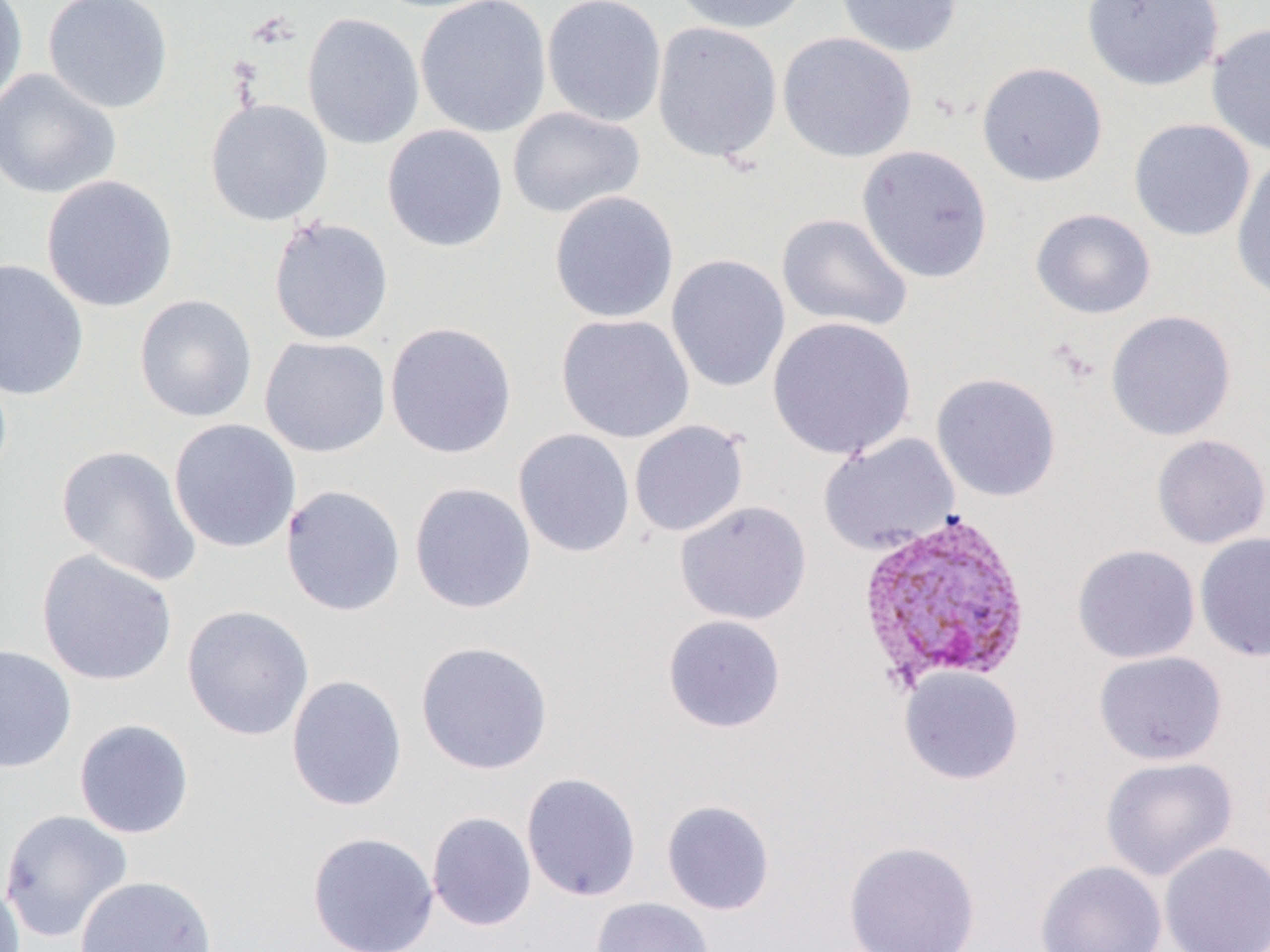

Summary:
  - Coordinate format: approximate bounding boxes as named x1/y1/x2/y2 corners in pixels
  - Uninfected red blood cell locations: (x1=0, y1=0, x2=29, y2=113), (x1=42, y1=0, x2=174, y2=115), (x1=414, y1=0, x2=552, y2=138), (x1=541, y1=0, x2=667, y2=128), (x1=670, y1=0, x2=812, y2=35), (x1=835, y1=0, x2=963, y2=58), (x1=1080, y1=0, x2=1224, y2=91), (x1=302, y1=12, x2=425, y2=150), (x1=651, y1=21, x2=783, y2=165), (x1=1206, y1=22, x2=1270, y2=157), (x1=777, y1=32, x2=917, y2=163), (x1=976, y1=61, x2=1108, y2=187), (x1=0, y1=69, x2=121, y2=200), (x1=205, y1=98, x2=334, y2=227), (x1=506, y1=106, x2=645, y2=219), (x1=1128, y1=118, x2=1256, y2=242), (x1=381, y1=124, x2=508, y2=252), (x1=856, y1=145, x2=994, y2=283), (x1=1231, y1=155, x2=1270, y2=303), (x1=40, y1=175, x2=178, y2=313), (x1=548, y1=191, x2=679, y2=324), (x1=1029, y1=208, x2=1157, y2=320), (x1=775, y1=212, x2=914, y2=333), (x1=268, y1=216, x2=394, y2=345), (x1=666, y1=253, x2=791, y2=392), (x1=0, y1=258, x2=89, y2=401), (x1=134, y1=294, x2=258, y2=423), (x1=1105, y1=310, x2=1237, y2=442), (x1=556, y1=313, x2=695, y2=443), (x1=767, y1=316, x2=916, y2=460), (x1=384, y1=321, x2=517, y2=460), (x1=259, y1=336, x2=391, y2=458), (x1=931, y1=372, x2=1061, y2=502), (x1=168, y1=418, x2=301, y2=554), (x1=629, y1=420, x2=749, y2=538), (x1=513, y1=428, x2=635, y2=558), (x1=818, y1=432, x2=961, y2=555), (x1=1151, y1=434, x2=1270, y2=549), (x1=55, y1=444, x2=202, y2=587), (x1=409, y1=482, x2=537, y2=614), (x1=280, y1=484, x2=407, y2=617), (x1=674, y1=500, x2=812, y2=625), (x1=1194, y1=531, x2=1270, y2=662), (x1=1072, y1=544, x2=1201, y2=664), (x1=35, y1=549, x2=179, y2=686), (x1=181, y1=604, x2=315, y2=741), (x1=662, y1=614, x2=786, y2=733), (x1=415, y1=640, x2=554, y2=776), (x1=0, y1=643, x2=78, y2=774), (x1=1093, y1=650, x2=1228, y2=765), (x1=899, y1=666, x2=1024, y2=785), (x1=285, y1=673, x2=408, y2=811), (x1=73, y1=718, x2=195, y2=839), (x1=1100, y1=755, x2=1238, y2=881), (x1=521, y1=772, x2=642, y2=902), (x1=661, y1=799, x2=775, y2=916), (x1=0, y1=809, x2=134, y2=943), (x1=426, y1=811, x2=537, y2=931), (x1=307, y1=831, x2=439, y2=952), (x1=843, y1=840, x2=981, y2=952), (x1=1158, y1=841, x2=1270, y2=952), (x1=1035, y1=859, x2=1167, y2=952), (x1=74, y1=874, x2=218, y2=952), (x1=0, y1=875, x2=26, y2=952), (x1=590, y1=896, x2=715, y2=952)
  - Plasmodium vivax-infected red blood cell locations: (x1=855, y1=509, x2=1033, y2=690)
  - Slide-level diagnosis: Plasmodium vivax
  - Field of view: single
  - Image size: 1270×952 pixels
  - Preparation: thin blood film
  - Magnification: 1000x
  - Modality: optical microscopy